Evaluate for malaria.
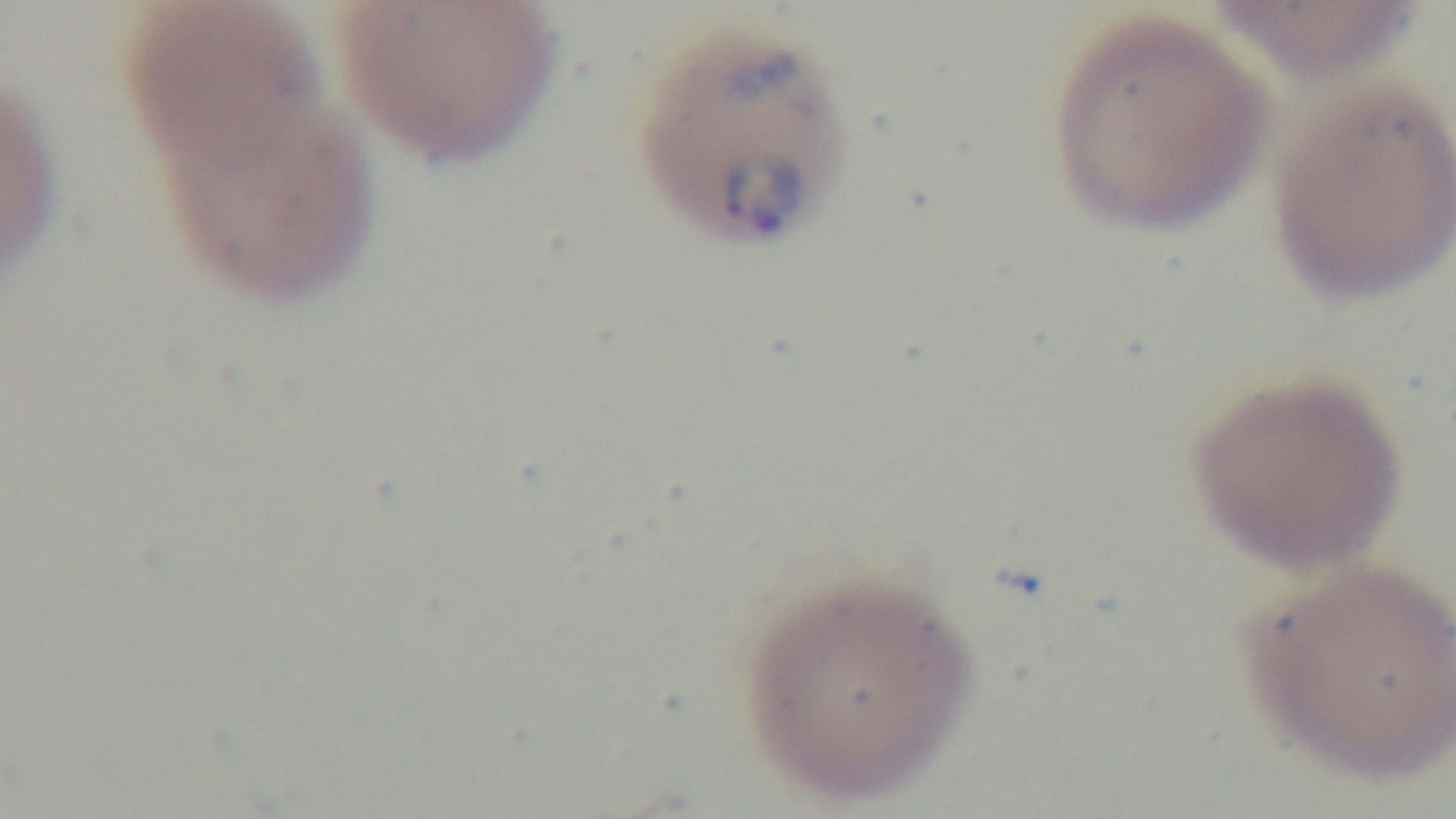
Infected.

Summary:
  - Modality: light microscopy
  - Stain: Giemsa
  - Objective: 100x oil immersion
  - Field of view: one from the slide
  - Preparation: thin smear
  - Capture: mounted 4K digital camera